Assess this cell for malaria.
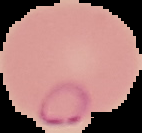
Parasitized.

image type = cell region segmented out of the field of view; surrounding area masked to black
preparation = thin blood film
image size = 142×133 pixels